Report the malaria status of this cell.
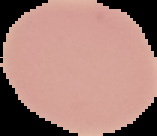

It is uninfected.

Summary:
  - Preparation: thin blood smear
  - Image type: segmented cell region on a black background
  - Image size: 157×136 pixels